Locate every Plasmodium parasite.
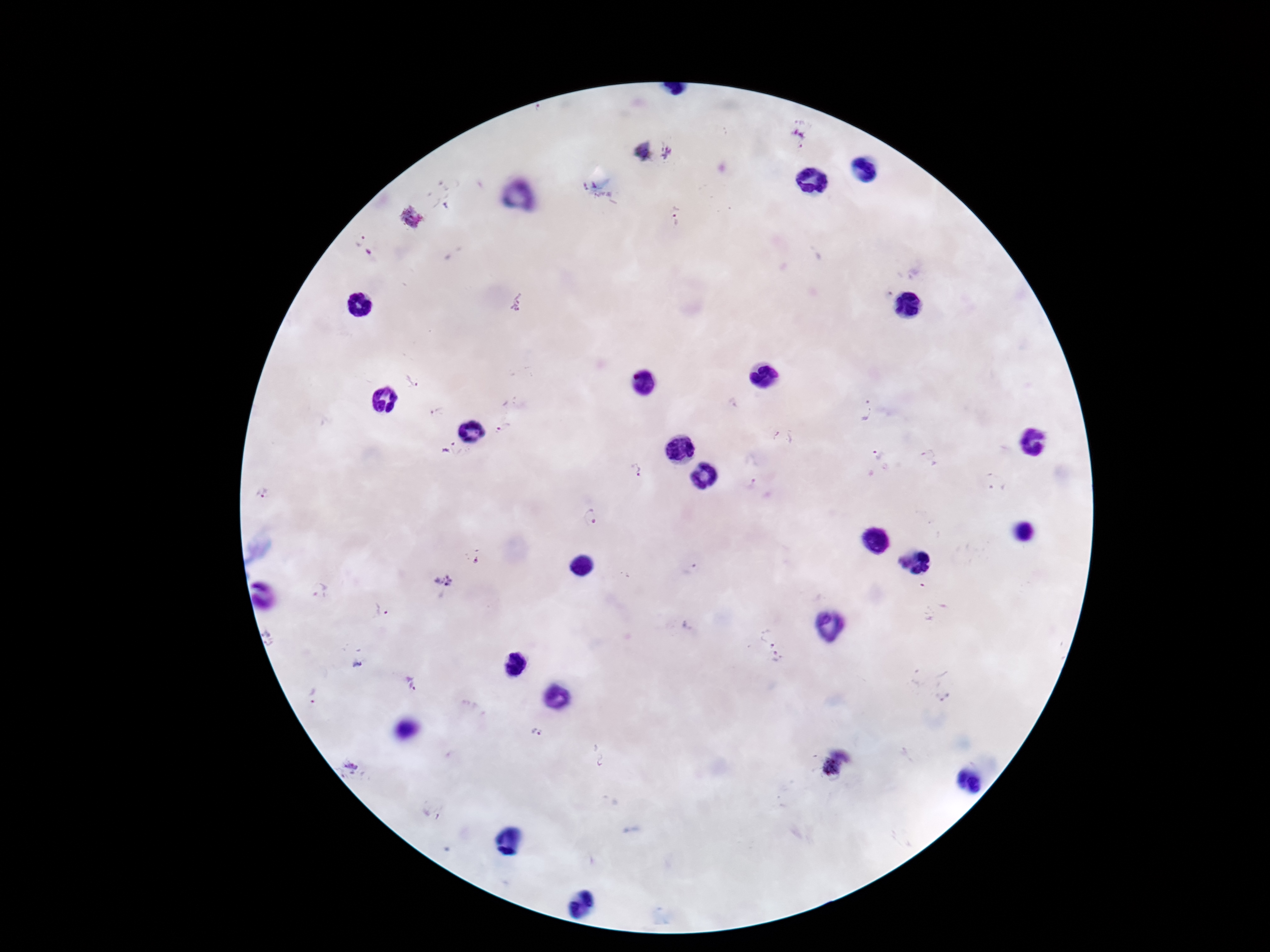
Approximate centers as [x, y] in pixels.
Plasmodium parasites: [802, 135], [641, 151], [669, 153], [589, 186], [676, 215], [411, 219], [360, 241], [368, 252], [518, 302], [413, 379], [864, 410], [436, 411], [502, 429], [782, 437], [447, 446], [876, 453], [928, 454], [636, 469], [996, 483], [750, 484], [590, 517], [472, 558], [443, 581], [318, 589], [381, 611], [269, 638], [768, 647], [914, 679], [414, 684], [947, 687], [313, 696], [536, 733], [352, 768], [833, 768].

Summary:
  - Preparation: thick peripheral-blood smear
  - Field of view: single
  - Magnification: 100x
  - Stain: Giemsa
  - Capture: smartphone camera through the microscope eyepiece
  - Image size: 1270×952 pixels
  - Patient malaria status: positive